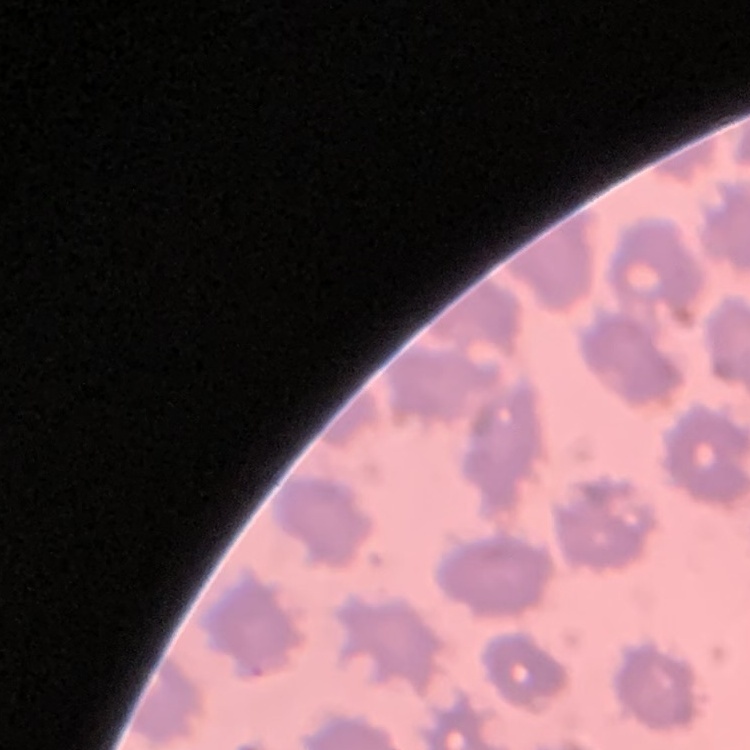
erythrocyte morphology = no rouleaux formation
image type = one tile cut from a larger photomicrograph
preparation = thin blood smear
stain = Field's or Giemsa